Report the malaria status of this cell.
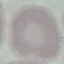
It is uninfected.

Cell patch, automatically extracted from a larger field of view and resized to 64 × 64 pixels. Acquired by smartphone through the microscope eyepiece. Giemsa-stained preparation. Thin smear of blood.